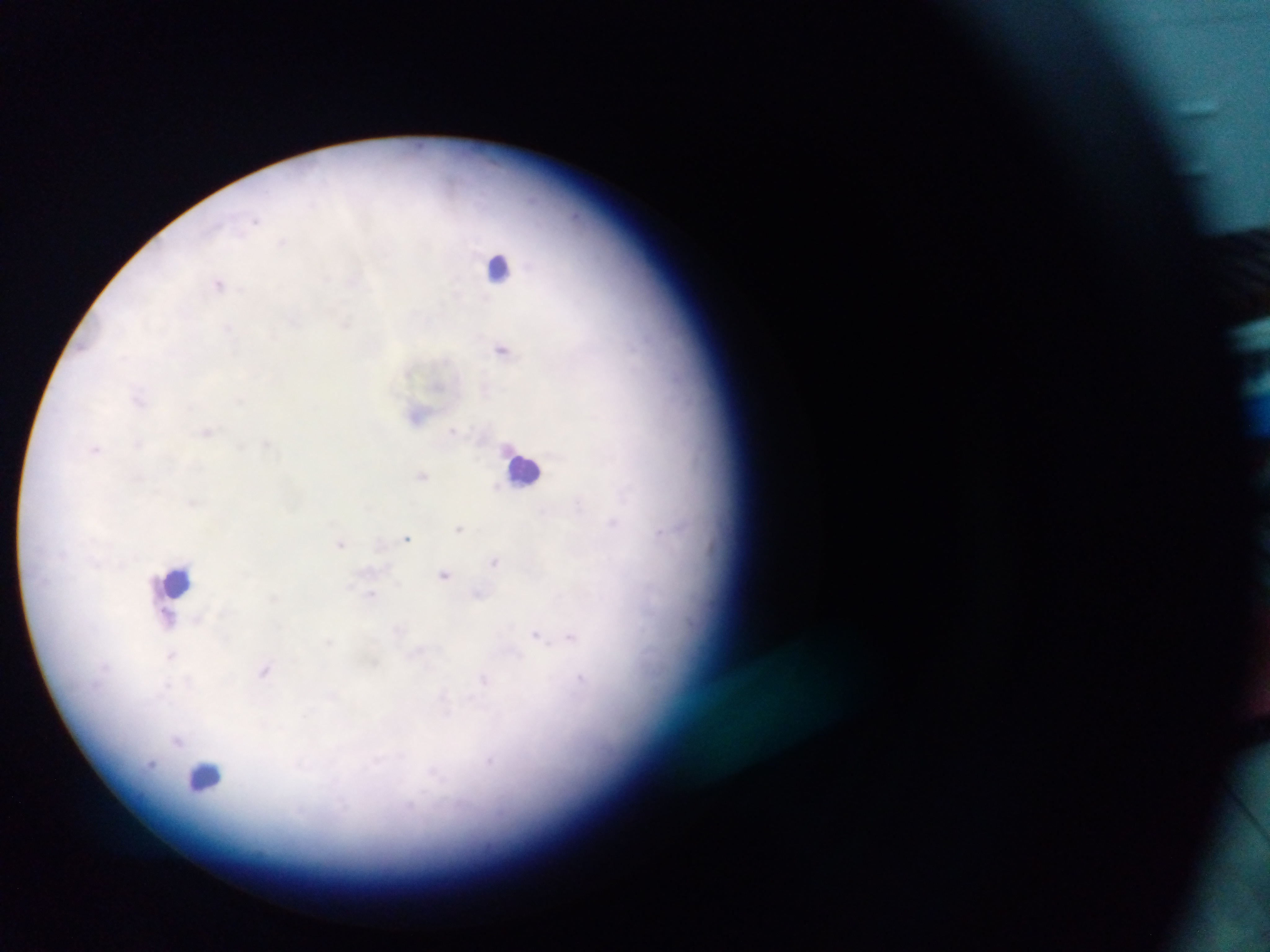
leukocyte locations = approximate centers as (x, y) in pixels: (501, 266), (523, 468), (178, 581), (206, 778)
field of view = single
capture = mobile-phone photograph through a microscope
image size = 1270×952 pixels
preparation = thick blood smear
Plasmodium parasite locations = approximate centers as (x, y) in pixels: (311, 205), (255, 219), (283, 241), (326, 279), (354, 280), (219, 284), (294, 322), (346, 322), (228, 327), (502, 349), (139, 399), (239, 401), (452, 430), (207, 431), (139, 443), (267, 444), (96, 449), (422, 475), (191, 503), (579, 503), (613, 522), (459, 528), (660, 533), (407, 538), (340, 543), (495, 561), (444, 574), (479, 594), (372, 595), (169, 618), (198, 620), (399, 631), (537, 635), (571, 637), (329, 642), (417, 655), (171, 656), (374, 662), (265, 670), (581, 678), (484, 681), (188, 683), (163, 688), (443, 699), (178, 741), (489, 761), (434, 773)
country = Ghana